Identify the cell.
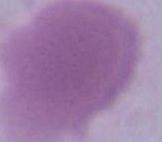

An erythrocyte.

Summary:
  - Magnification: 1000x
  - Modality: micrograph